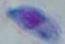

Micrograph. Toxoplasma gondii is seen. Captured at 1000x magnification.